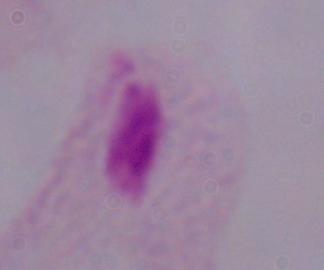 1000x magnification. A trichomonad is shown. Photomicrograph.